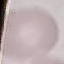

Summary:
  - Malaria status: uninfected
  - Preparation: thin blood smear
  - Stain: Giemsa
  - Capture: smartphone through the microscope eyepiece
  - Image type: automatically extracted cell patch, resized to 64 × 64 pixels